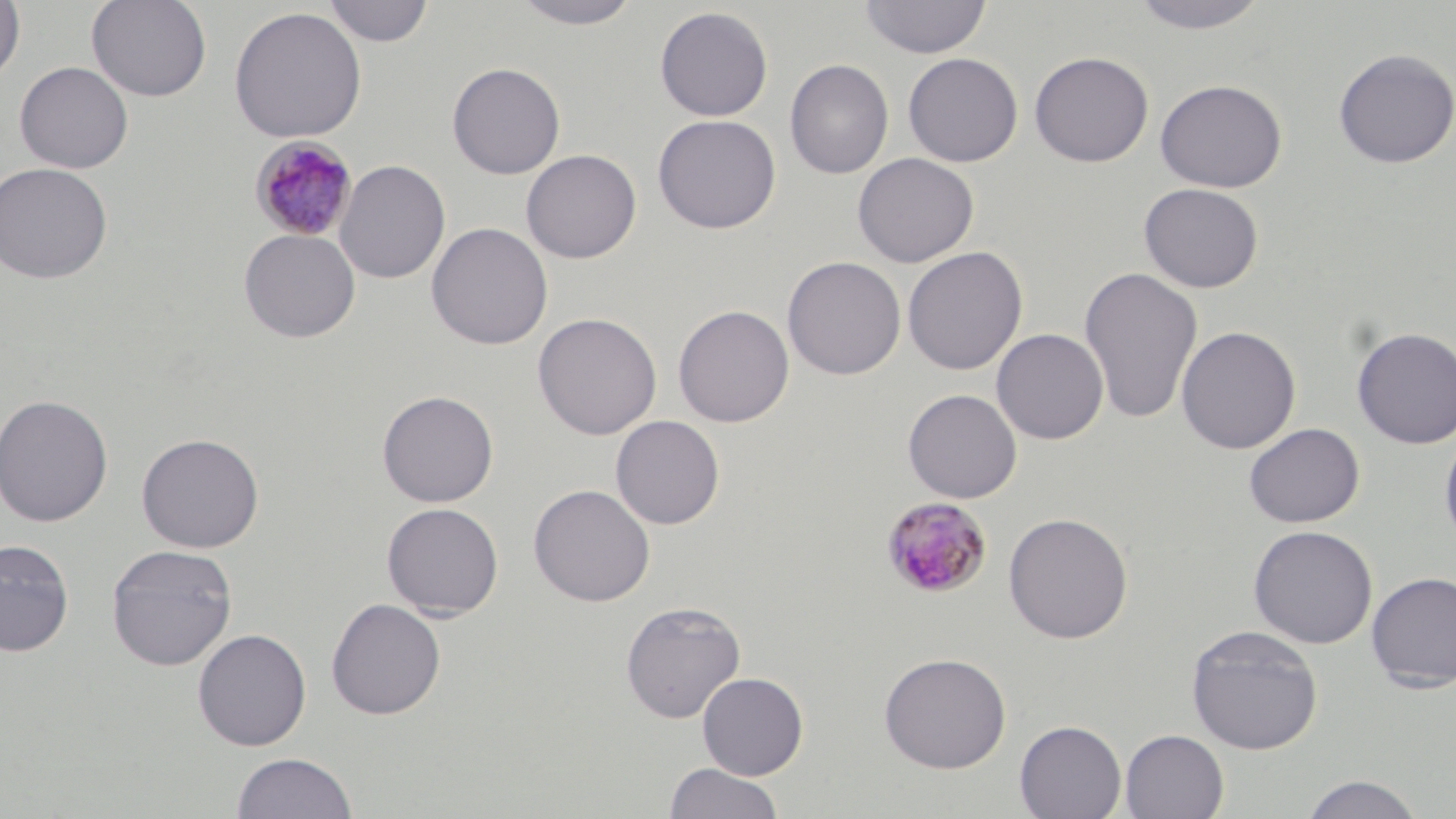
slide_level_diagnosis: Plasmodium malariae
stain: May-Grünwald-Giemsa
image_size: 1456×819 pixels
uninfected_red_blood_cell_locations: 'approximate bounding boxes as named x1/y1/x2/y2 corners in pixels: (x1=0, y1=0, x2=25, y2=86), (x1=86, y1=0, x2=212, y2=102), (x1=322, y1=0, x2=435, y2=47), (x1=510, y1=0, x2=645, y2=29), (x1=859, y1=0, x2=992, y2=59), (x1=1127, y1=0, x2=1273, y2=35), (x1=228, y1=6, x2=367, y2=143), (x1=654, y1=6, x2=773, y2=121), (x1=1332, y1=47, x2=1455, y2=169), (x1=1029, y1=51, x2=1154, y2=167), (x1=903, y1=52, x2=1023, y2=167), (x1=785, y1=59, x2=894, y2=180), (x1=14, y1=60, x2=133, y2=173), (x1=446, y1=62, x2=566, y2=179), (x1=1154, y1=78, x2=1287, y2=193), (x1=652, y1=114, x2=781, y2=234), (x1=521, y1=149, x2=641, y2=263), (x1=852, y1=152, x2=979, y2=268), (x1=334, y1=160, x2=450, y2=284), (x1=0, y1=162, x2=113, y2=283), (x1=1138, y1=182, x2=1264, y2=293), (x1=426, y1=222, x2=554, y2=350), (x1=239, y1=228, x2=361, y2=343), (x1=902, y1=246, x2=1028, y2=376), (x1=782, y1=256, x2=906, y2=380), (x1=1079, y1=266, x2=1204, y2=425), (x1=673, y1=304, x2=795, y2=427), (x1=532, y1=312, x2=662, y2=440), (x1=1176, y1=325, x2=1301, y2=454), (x1=1351, y1=326, x2=1456, y2=449), (x1=991, y1=328, x2=1109, y2=445), (x1=902, y1=389, x2=1022, y2=503), (x1=377, y1=390, x2=499, y2=507), (x1=0, y1=394, x2=113, y2=527), (x1=611, y1=415, x2=725, y2=529), (x1=1244, y1=422, x2=1364, y2=528), (x1=1439, y1=428, x2=1456, y2=549), (x1=136, y1=433, x2=264, y2=553), (x1=528, y1=484, x2=655, y2=606), (x1=381, y1=502, x2=504, y2=619), (x1=1003, y1=512, x2=1134, y2=643), (x1=1247, y1=524, x2=1378, y2=649), (x1=0, y1=538, x2=74, y2=656), (x1=106, y1=544, x2=237, y2=671), (x1=1365, y1=570, x2=1456, y2=693), (x1=326, y1=598, x2=446, y2=720), (x1=621, y1=601, x2=746, y2=724), (x1=1186, y1=625, x2=1323, y2=754), (x1=193, y1=628, x2=311, y2=751), (x1=878, y1=651, x2=1012, y2=773), (x1=697, y1=672, x2=808, y2=779), (x1=1014, y1=720, x2=1127, y2=819), (x1=1119, y1=729, x2=1229, y2=818), (x1=231, y1=751, x2=358, y2=818), (x1=663, y1=762, x2=785, y2=819), (x1=1298, y1=773, x2=1425, y2=819)'
modality: light microscopy
plasmodium_malariae_infected_red_blood_cell_locations: 'approximate bounding boxes as named x1/y1/x2/y2 corners in pixels: (x1=248, y1=135, x2=359, y2=241), (x1=880, y1=496, x2=993, y2=598)'
preparation: thin blood smear
magnification: 1000x
field_of_view: single